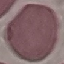
Result: no malaria parasites seen. Automatically extracted cell patch, resized to 64 × 64 pixels. Giemsa-stained preparation. Acquired by smartphone through the microscope eyepiece. Thin smear of blood.